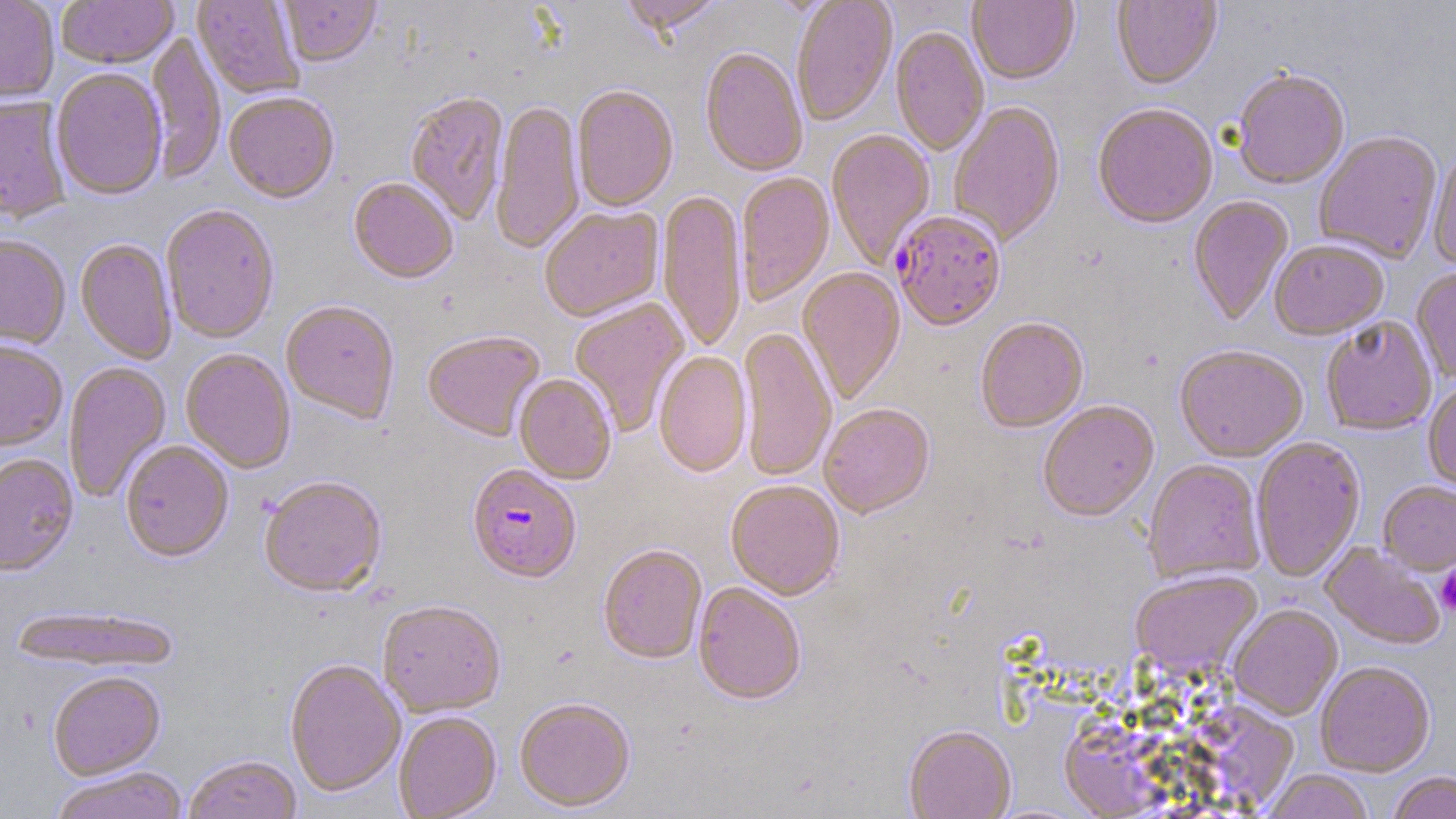
slide_level_diagnosis: Plasmodium falciparum
stain: May-Grünwald-Giemsa
magnification: 1000x
preparation: thin blood film
plasmodium_falciparum_infected_red_blood_cell_locations: 'approximate bounding boxes as (x1,y1)-(x2,y2) corner pairs in pixels: (891,212)-(1007,334), (467,467)-(581,586)'
modality: optical microscopy
platelet_locations: 'approximate bounding boxes as (x1,y1)-(x2,y2) corner pairs in pixels: (1436,568)-(1456,615)'
image_size: 1456×819 pixels
uninfected_red_blood_cell_locations: 'approximate bounding boxes as (x1,y1)-(x2,y2) corner pairs in pixels: (0,0)-(59,104), (57,0)-(177,70), (191,0)-(305,100), (279,0)-(381,69), (620,0)-(726,40), (792,0)-(897,128), (967,0)-(1079,87), (1112,1)-(1222,92), (890,27)-(989,157), (147,31)-(226,186), (700,49)-(808,179), (51,69)-(167,202), (1231,72)-(1350,191), (572,87)-(678,214), (224,94)-(339,206), (405,94)-(510,226), (0,97)-(71,226), (491,101)-(584,256), (949,103)-(1066,248), (1093,106)-(1218,232), (826,130)-(936,269), (1314,132)-(1443,264), (1429,147)-(1456,271), (736,173)-(835,307), (348,180)-(458,286), (658,191)-(746,354), (1188,196)-(1295,327), (160,206)-(279,345), (540,208)-(664,323), (0,237)-(70,350), (75,240)-(177,365), (1270,242)-(1388,342), (797,268)-(907,406), (1411,270)-(1456,382), (570,299)-(690,437), (281,302)-(399,426), (975,319)-(1089,435), (1321,319)-(1436,437), (738,327)-(836,484), (422,332)-(546,444), (0,343)-(67,453), (1174,347)-(1307,465), (181,350)-(295,474), (654,352)-(752,479), (63,361)-(172,503), (514,375)-(616,486), (1423,383)-(1456,494), (1039,403)-(1159,525), (820,405)-(936,521), (1251,438)-(1366,584), (120,442)-(234,564), (0,455)-(79,579), (1143,460)-(1265,586), (259,478)-(388,600), (725,482)-(845,603), (1377,482)-(1456,576), (1319,544)-(1446,651), (598,546)-(707,666), (1131,572)-(1263,681), (693,584)-(805,708), (378,603)-(506,719), (9,605)-(181,675), (1228,605)-(1343,722), (285,660)-(406,800), (1315,663)-(1434,778), (48,673)-(166,782), (515,700)-(635,814), (394,712)-(501,819), (903,727)-(1016,819), (183,756)-(303,819), (51,769)-(189,819), (1262,770)-(1374,819), (1387,772)-(1456,819)'
field_of_view: one of a larger specimen